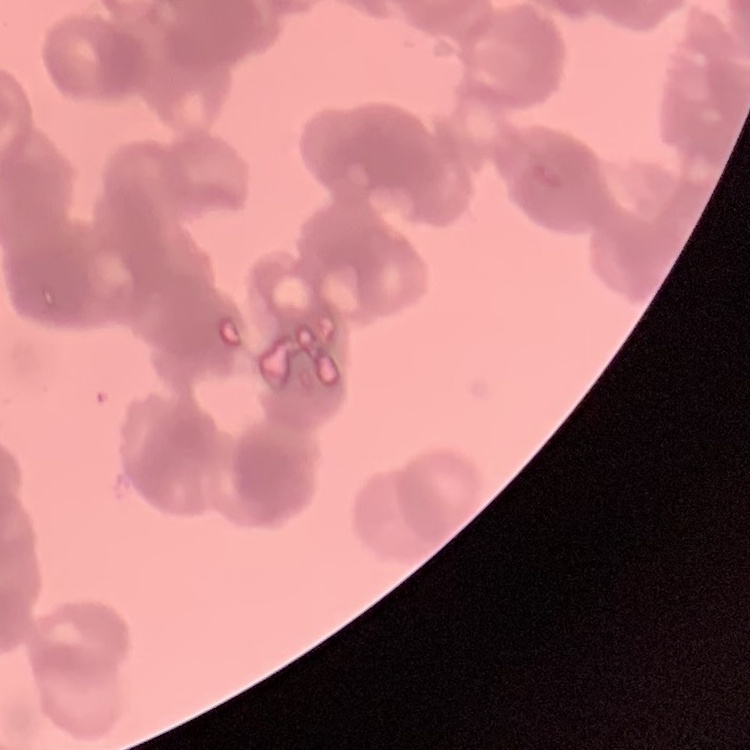
The red blood cells show rouleaux formation. One tile cut from a larger photomicrograph. Thin blood smear. Stained with either Field's or Giemsa.